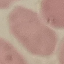
Malaria status: uninfected. Automatically extracted cell patch, resized to 64 × 64 pixels. Thin blood smear. Giemsa stain. Acquired by smartphone through the microscope eyepiece.